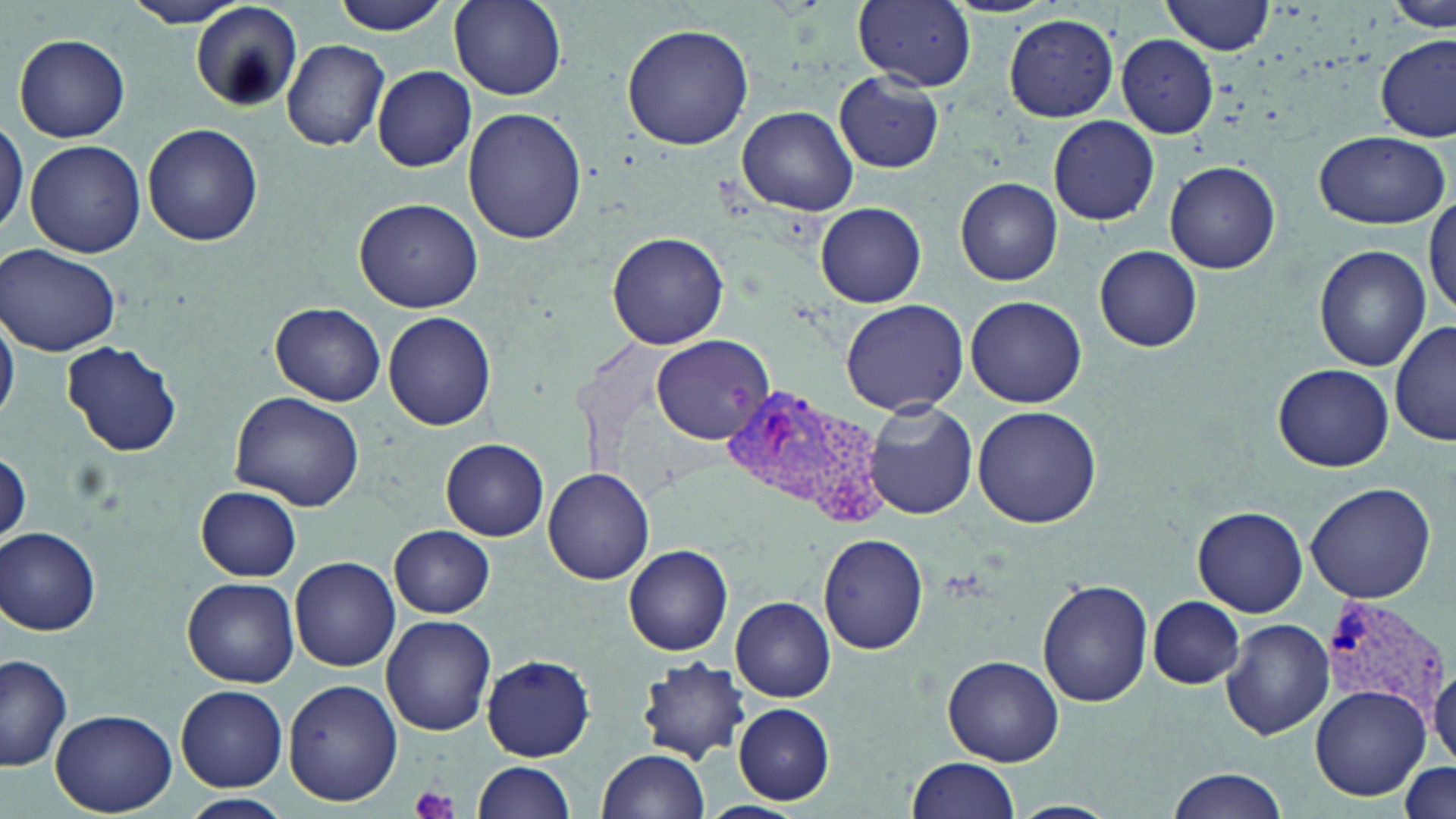
Summary:
  - Coordinate format: approximate bounding boxes as named x1/y1/x2/y2 corners in pixels
  - Platelet locations: (x1=410, y1=784, x2=457, y2=819)
  - Uninfected red blood cell locations: (x1=121, y1=0, x2=257, y2=28), (x1=329, y1=0, x2=452, y2=35), (x1=447, y1=0, x2=566, y2=100), (x1=851, y1=0, x2=979, y2=92), (x1=1163, y1=0, x2=1275, y2=55), (x1=1390, y1=0, x2=1453, y2=31), (x1=191, y1=4, x2=303, y2=110), (x1=1004, y1=14, x2=1119, y2=122), (x1=621, y1=23, x2=753, y2=151), (x1=14, y1=33, x2=130, y2=142), (x1=1117, y1=34, x2=1219, y2=138), (x1=1378, y1=36, x2=1455, y2=140), (x1=281, y1=39, x2=389, y2=151), (x1=372, y1=65, x2=477, y2=171), (x1=834, y1=74, x2=944, y2=172), (x1=737, y1=105, x2=859, y2=216), (x1=463, y1=107, x2=588, y2=247), (x1=0, y1=113, x2=27, y2=244), (x1=1047, y1=115, x2=1160, y2=225), (x1=144, y1=125, x2=265, y2=248), (x1=1312, y1=130, x2=1451, y2=228), (x1=24, y1=139, x2=146, y2=257), (x1=1165, y1=161, x2=1282, y2=275), (x1=956, y1=177, x2=1063, y2=286), (x1=356, y1=199, x2=484, y2=311), (x1=1426, y1=199, x2=1456, y2=320), (x1=816, y1=203, x2=926, y2=307), (x1=607, y1=231, x2=729, y2=350), (x1=1, y1=244, x2=122, y2=356), (x1=1095, y1=246, x2=1202, y2=352), (x1=1315, y1=246, x2=1430, y2=369), (x1=966, y1=295, x2=1088, y2=408), (x1=841, y1=299, x2=968, y2=415), (x1=271, y1=302, x2=386, y2=406), (x1=0, y1=303, x2=19, y2=428), (x1=383, y1=312, x2=496, y2=430), (x1=1391, y1=320, x2=1454, y2=450), (x1=649, y1=334, x2=773, y2=445), (x1=61, y1=340, x2=184, y2=458), (x1=1273, y1=362, x2=1394, y2=472), (x1=230, y1=389, x2=367, y2=513), (x1=863, y1=401, x2=977, y2=520), (x1=973, y1=406, x2=1101, y2=530), (x1=441, y1=438, x2=549, y2=540), (x1=1, y1=450, x2=31, y2=545), (x1=541, y1=466, x2=655, y2=584), (x1=1305, y1=481, x2=1436, y2=603), (x1=196, y1=487, x2=302, y2=580), (x1=1192, y1=506, x2=1308, y2=617), (x1=390, y1=524, x2=495, y2=616), (x1=2, y1=527, x2=102, y2=635), (x1=819, y1=534, x2=929, y2=654), (x1=625, y1=546, x2=733, y2=654), (x1=290, y1=556, x2=401, y2=672), (x1=183, y1=576, x2=299, y2=687), (x1=1038, y1=577, x2=1154, y2=707), (x1=1149, y1=596, x2=1245, y2=689), (x1=731, y1=597, x2=835, y2=702), (x1=382, y1=615, x2=496, y2=736), (x1=1222, y1=618, x2=1335, y2=739), (x1=0, y1=653, x2=73, y2=773), (x1=943, y1=654, x2=1065, y2=766), (x1=480, y1=655, x2=593, y2=760), (x1=637, y1=658, x2=750, y2=766), (x1=1428, y1=663, x2=1456, y2=768), (x1=282, y1=678, x2=401, y2=806), (x1=176, y1=685, x2=288, y2=792), (x1=1310, y1=685, x2=1432, y2=801), (x1=734, y1=704, x2=834, y2=804), (x1=52, y1=708, x2=176, y2=816), (x1=598, y1=749, x2=711, y2=819), (x1=906, y1=756, x2=1020, y2=818), (x1=471, y1=761, x2=576, y2=818), (x1=1399, y1=761, x2=1453, y2=818), (x1=1166, y1=770, x2=1289, y2=819), (x1=181, y1=793, x2=291, y2=819), (x1=696, y1=801, x2=807, y2=819), (x1=1007, y1=801, x2=1121, y2=819)
  - Plasmodium vivax-infected red blood cell locations: (x1=722, y1=387, x2=888, y2=523), (x1=1320, y1=595, x2=1448, y2=725)
  - Slide-level diagnosis: Plasmodium vivax
  - Field of view: one of a larger specimen
  - Magnification: 1000x
  - Stain: May-Grünwald-Giemsa
  - Preparation: thin blood smear
  - Image size: 1456×819 pixels
  - Modality: optical microscopy